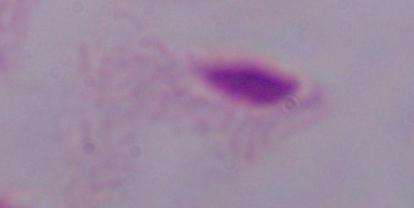

Captured at 1000x magnification. A trichomonad is seen. Micrograph.